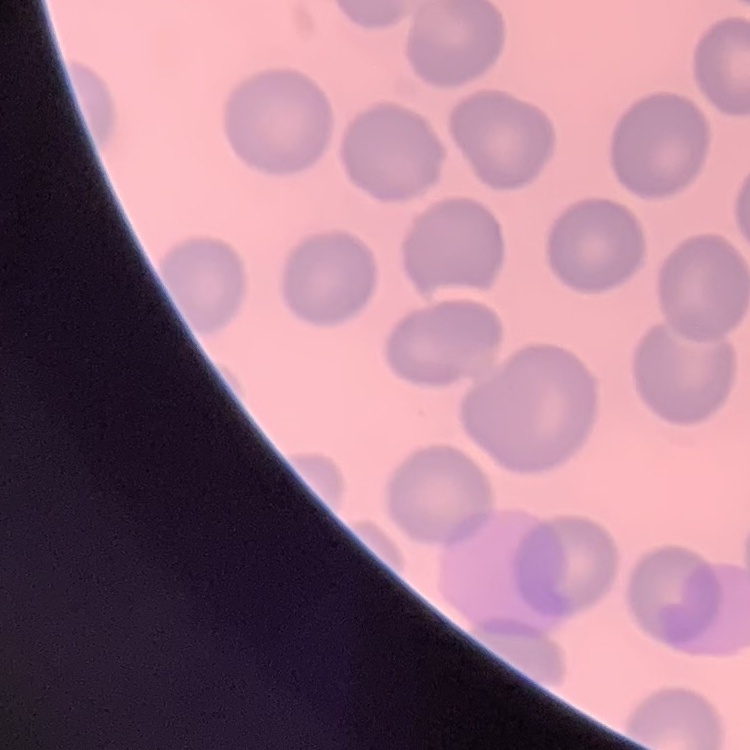
Summary:
  - Erythrocyte morphology: no rouleaux formation
  - Stain: Field's or Giemsa
  - Preparation: thin blood smear
  - Image type: one tile cut from a larger photomicrograph